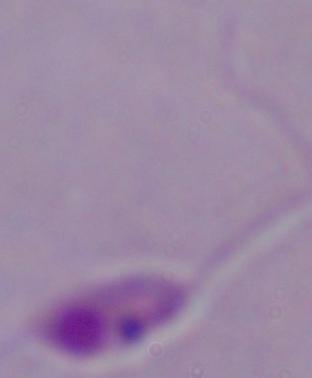

identification = Leishmania
modality = micrograph
magnification = 1000x